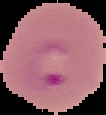
image type = segmented cell region with the area outside set to black
image size = 106×115 pixels
malaria status = parasitized
preparation = thin blood film